Assess for malaria.
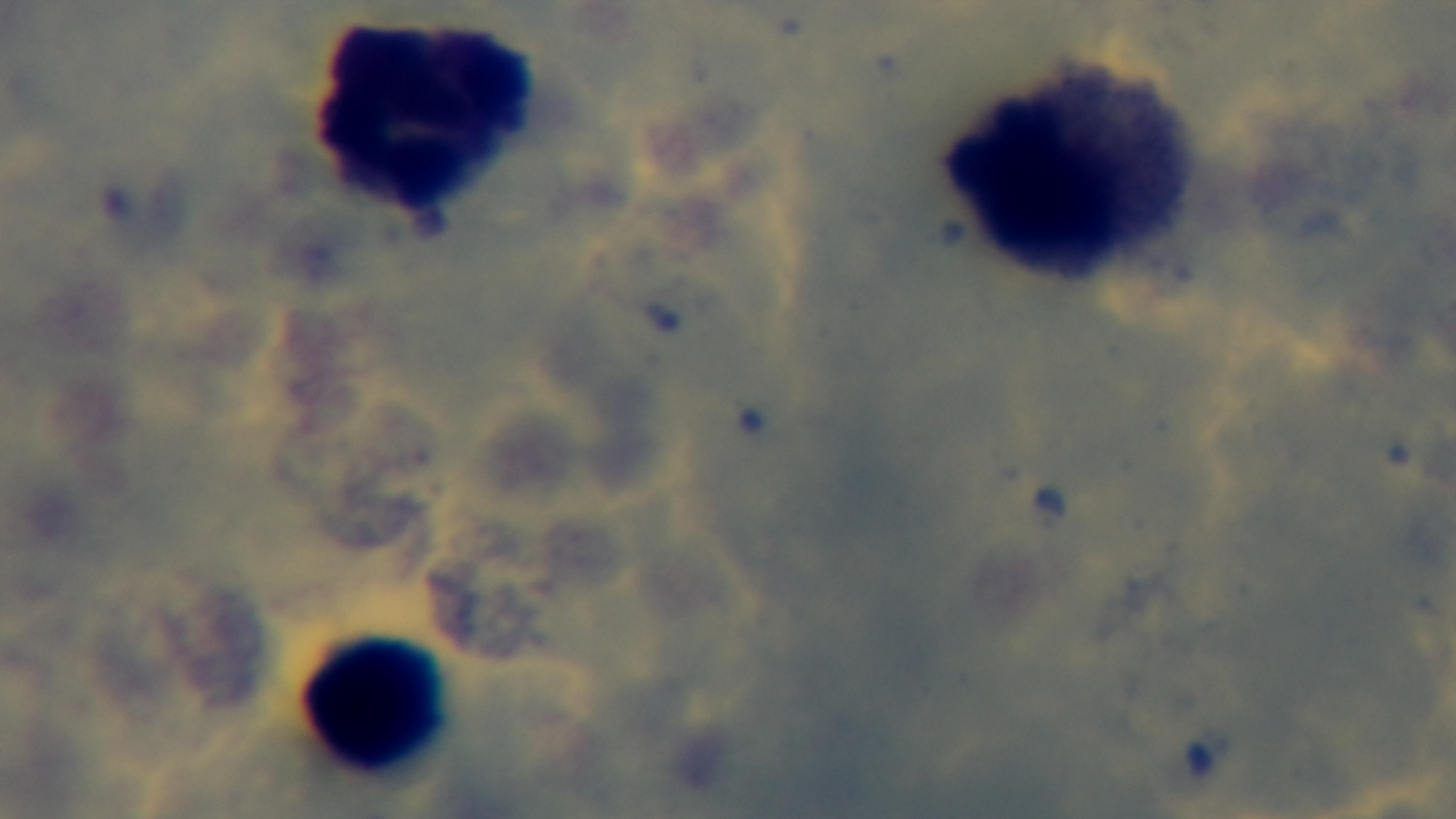
Negative.

Oil-immersion objective, 100x. Giemsa-stained. Single field of view. Mounted 4K digital camera. Photomicrograph. Preparation: thick smear.